Give the position of every Plasmodium parasite visible.
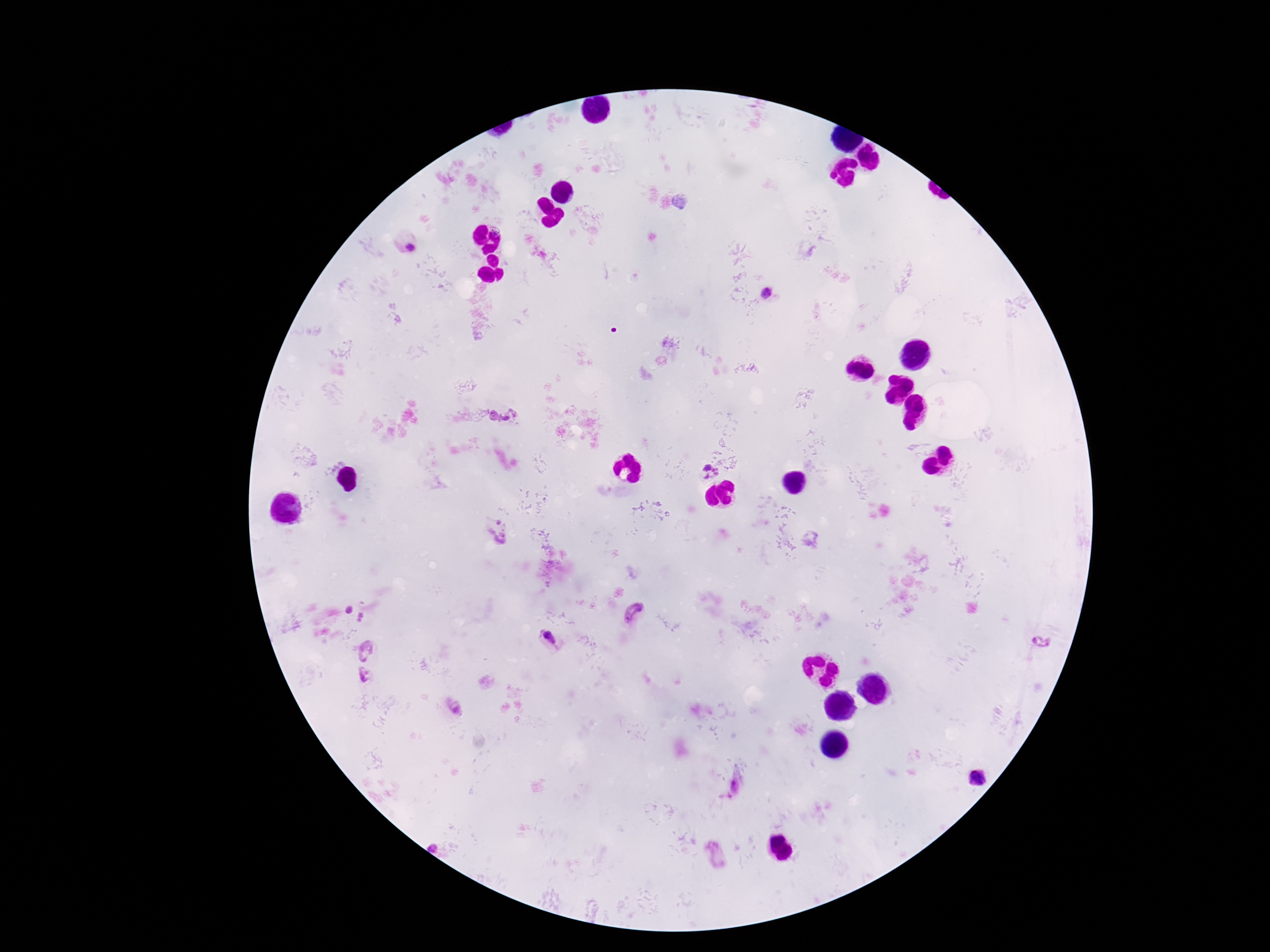

Approximate centers as {x, y} in pixels.
Plasmodium parasites: {412, 248}, {767, 294}, {503, 413}, {707, 467}, {717, 471}, {706, 476}, {498, 530}, {349, 610}, {635, 614}, {362, 618}, {549, 638}, {1042, 640}, {366, 649}, {364, 676}, {977, 778}.

Photographed through the microscope eyepiece with a smartphone camera. 100x magnification. Image is 1270×952 pixels. Giemsa-stained preparation. Thick blood film. Patient malaria status: positive. Single field of view.